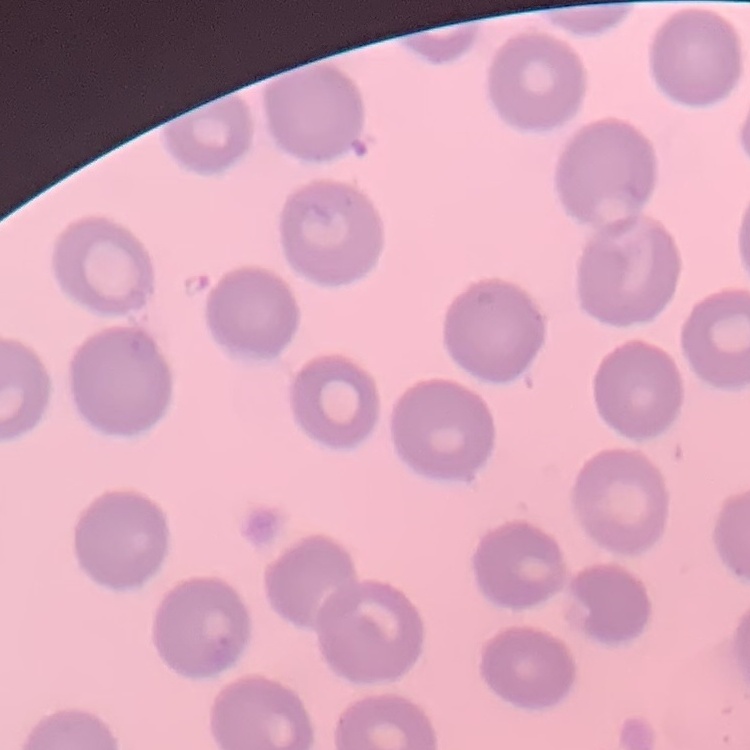

{
  "red_blood_cell_morphology": "no rouleaux formation",
  "image_type": "one tile cut from a larger photomicrograph",
  "preparation": "thin blood smear",
  "stain": "Field's or Giemsa"
}